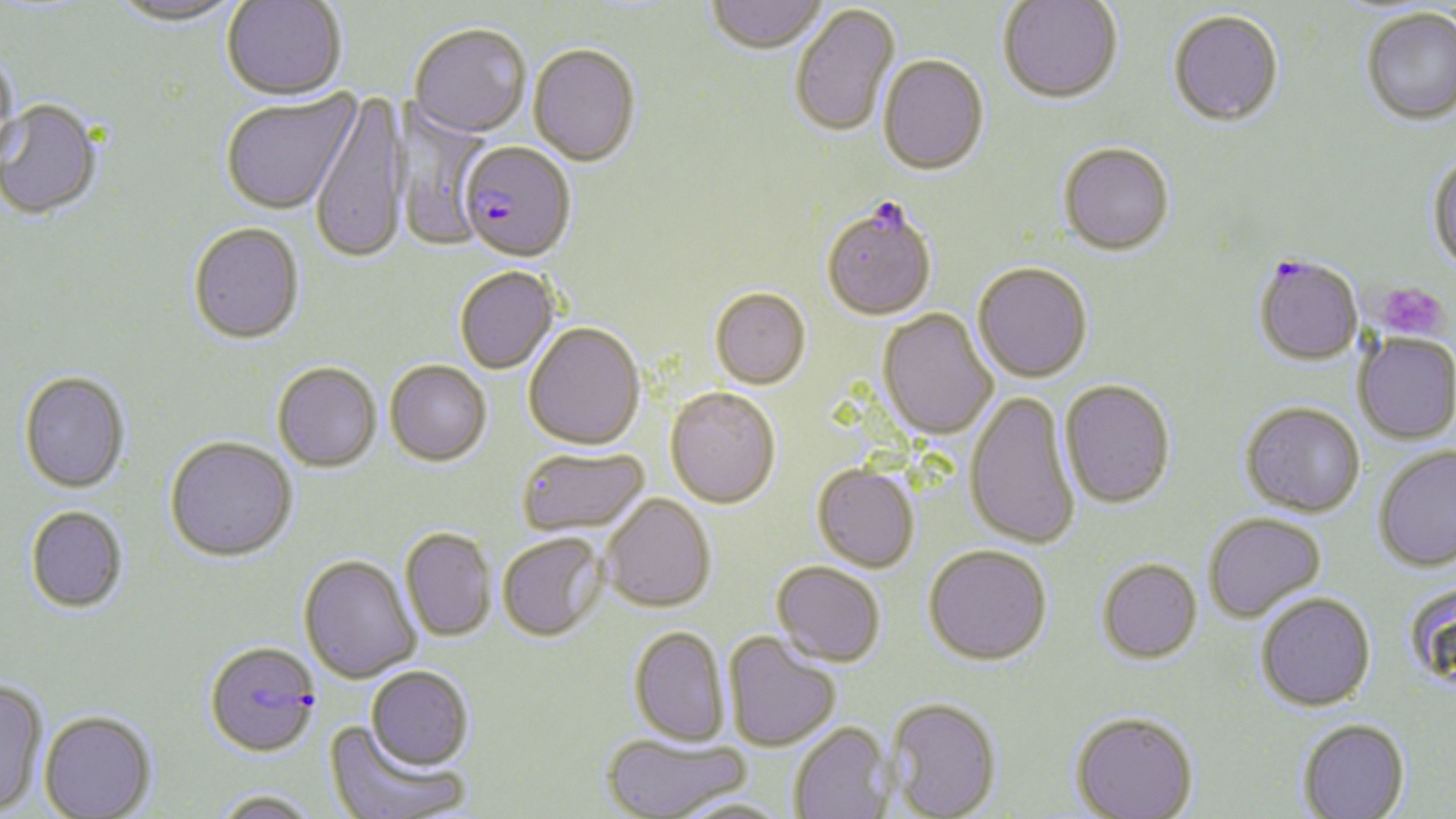
Summary:
  - Coordinate format: approximate bounding boxes as (x1,y1)-(x2,y2) corner pairs in pixels
  - Plasmodium falciparum-infected red blood cell locations (subset): (458,140)-(576,261), (1254,257)-(1363,366), (204,640)-(321,756)
  - Uninfected red blood cell locations (subset): (108,0)-(246,26), (223,0)-(347,99), (706,0)-(827,53), (998,0)-(1122,104), (790,3)-(900,138), (1361,9)-(1456,127), (1169,11)-(1284,129), (408,22)-(531,137), (529,43)-(641,165), (1,48)-(20,165), (878,55)-(989,175), (220,90)-(360,214), (309,91)-(409,265), (0,98)-(102,219), (391,100)-(492,252), (1059,143)-(1175,257), (1426,155)-(1456,274), (188,222)-(305,343), (973,262)-(1093,383), (454,266)-(559,374), (710,286)-(811,388), (878,310)-(998,440), (523,321)-(645,449), (1353,332)-(1456,445), (385,360)-(492,465), (272,361)-(382,471), (19,370)-(131,492), (1059,380)-(1176,509), (665,386)-(781,508), (965,390)-(1080,551), (1241,402)-(1365,517), (165,435)-(298,561), (1374,445)-(1456,572), (516,446)-(649,535), (813,464)-(920,572), (601,493)-(715,612), (25,505)-(129,613), (1203,512)-(1326,622), (400,527)-(496,642), (498,531)-(608,641), (923,544)-(1052,665), (298,553)-(421,683), (1097,559)-(1202,664), (772,561)-(886,666), (1404,581)-(1456,691), (1256,592)-(1375,711), (629,626)-(730,746), (723,631)-(841,752), (366,666)-(474,770), (0,678)-(48,814), (887,697)-(1003,818), (39,710)-(156,818), (1070,712)-(1199,819), (1297,719)-(1410,819), (324,721)-(469,819), (789,721)-(894,819), (602,734)-(751,818), (213,790)-(321,819), (674,797)-(796,819)
  - Platelet locations: (1374,281)-(1451,342)
  - Slide-level diagnosis: Plasmodium falciparum
  - Image size: 1456×819 pixels
  - Field of view: one of a larger specimen
  - Magnification: 1000x
  - Preparation: thin blood smear
  - Modality: optical microscopy
  - Stain: May-Grünwald-Giemsa